Identify the cell.
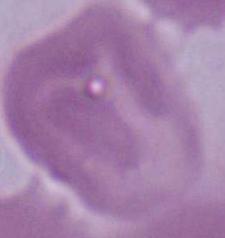

This is an erythrocyte.

magnification = 1000x
modality = micrograph